Report the malaria status of this cell.
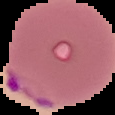
Parasitized.

Summary:
  - Image type: segmented cell region with the area outside set to black
  - Image size: 115×115 pixels
  - Preparation: thin blood smear